Classify this cell by malaria status.
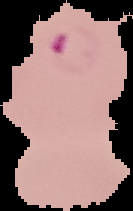
It is parasitized.

Summary:
  - Image size: 133×211 pixels
  - Preparation: thin blood film
  - Image type: cell region segmented out of the field of view; surrounding area masked to black